State which parasite is depicted.
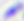

This is Toxoplasma gondii.

Micrograph. Captured at 400x magnification.